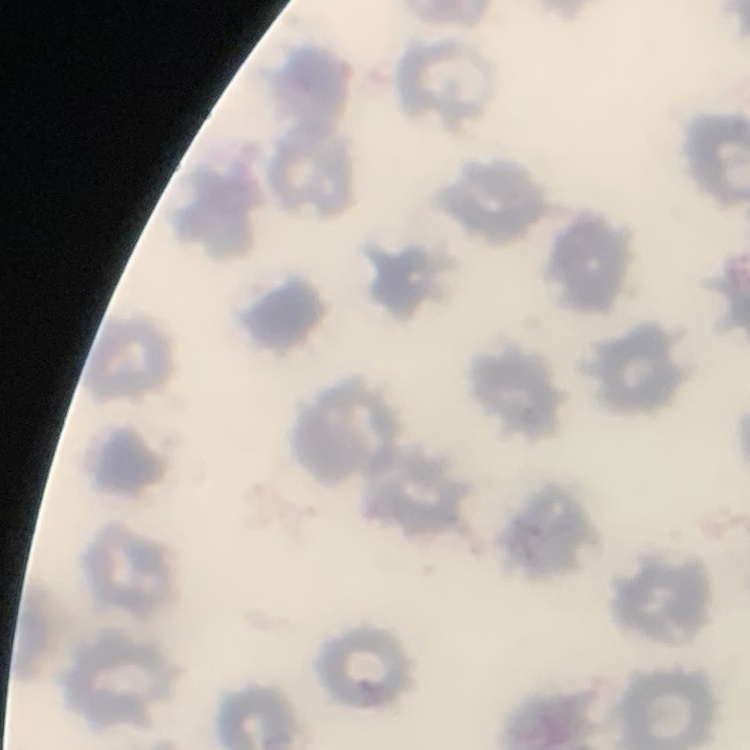

Summary:
  - Erythrocyte morphology: no rouleaux formation
  - Stain: Field's or Giemsa
  - Preparation: thin blood film
  - Image type: square crop of a larger photomicrograph